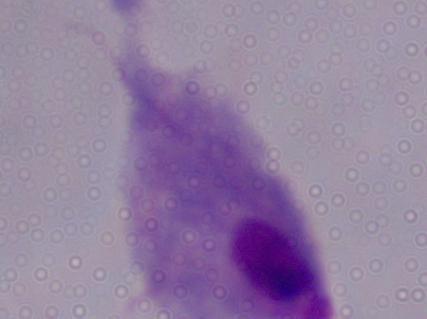
Summary:
  - Identification: trichomonad
  - Modality: photomicrograph
  - Magnification: 1000x